Describe the morphology of the erythrocytes.
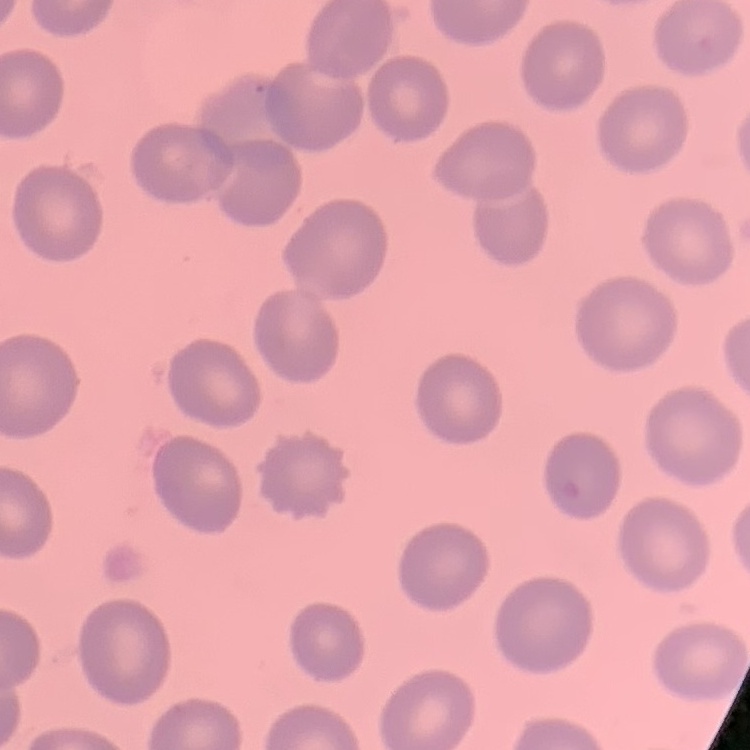

They show no rouleaux formation.

{
  "stain": "Field's or Giemsa",
  "image_type": "square crop of a larger photomicrograph",
  "preparation": "thin blood film"
}